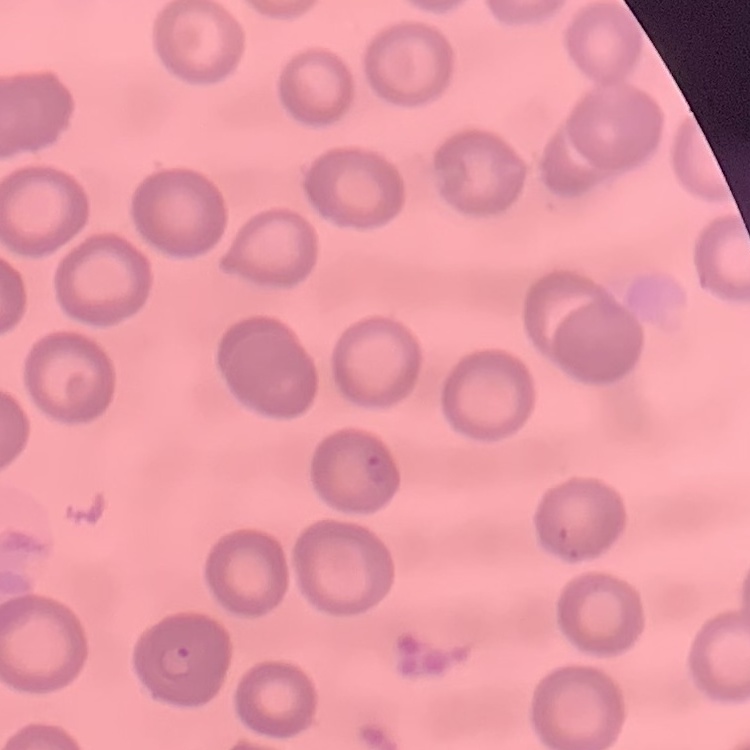 The erythrocytes show no rouleaux formation. Thin peripheral smear. One tile cut from a larger photomicrograph. Stained with either Field's or Giemsa.